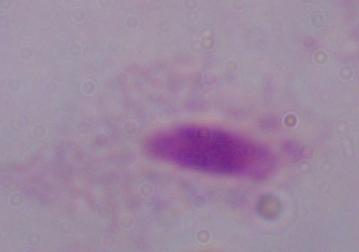

modality: photomicrograph
magnification: 1000x
identification: trichomonad